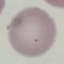
Summary:
  - Malaria status: uninfected
  - Stain: Giemsa
  - Capture: smartphone camera at the microscope eyepiece
  - Image type: cell patch, automatically extracted from a larger field of view and resized to 64 × 64 pixels
  - Preparation: thin blood smear